Report the malaria status of this cell.
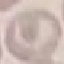
Uninfected.

Summary:
  - Image type: automatically extracted cell patch, resized to 64 × 64 pixels
  - Preparation: thin smear
  - Stain: Giemsa
  - Capture: smartphone camera at the microscope eyepiece